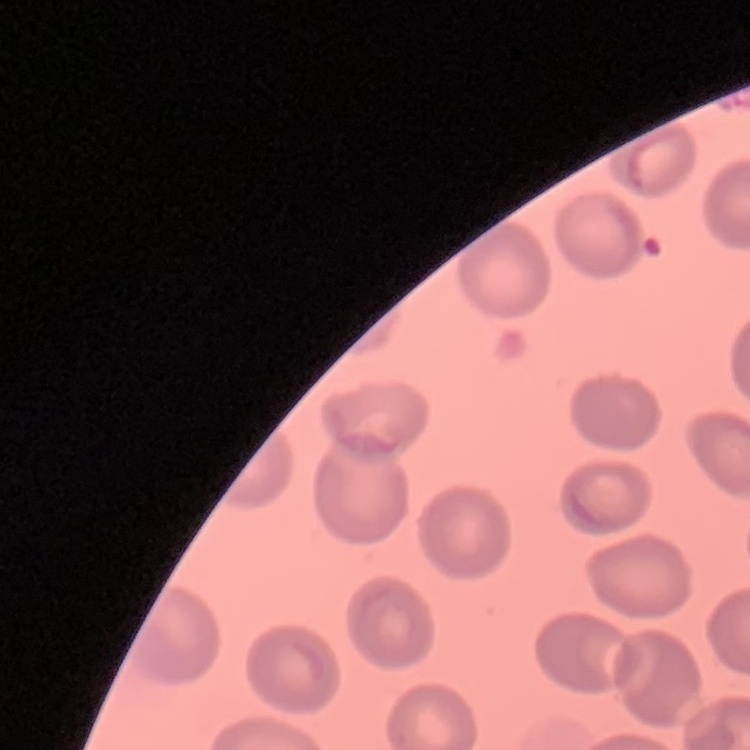

red blood cell morphology = no rouleaux formation
image type = square crop of a larger photomicrograph
stain = Field's or Giemsa
preparation = thin peripheral smear